Report the malaria status of this cell.
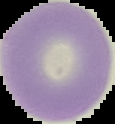
It is uninfected.

Summary:
  - Image type: segmented cell region on a black background
  - Preparation: thin blood film
  - Image size: 115×124 pixels